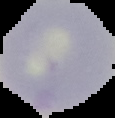

From a thin blood film. Result: no Plasmodium parasites seen. Cell region segmented out of the field of view; the surrounding area is masked to black. Image is 115×118 pixels.